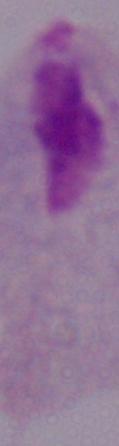
A trichomonad is seen. Captured at 1000x magnification. Micrograph.